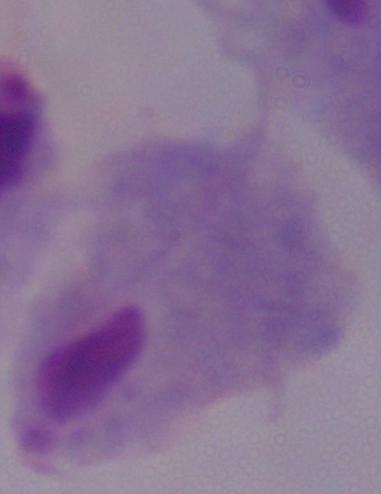
1000x magnification. Photomicrograph. A trichomonad is seen.